Describe the morphology of the erythrocytes.
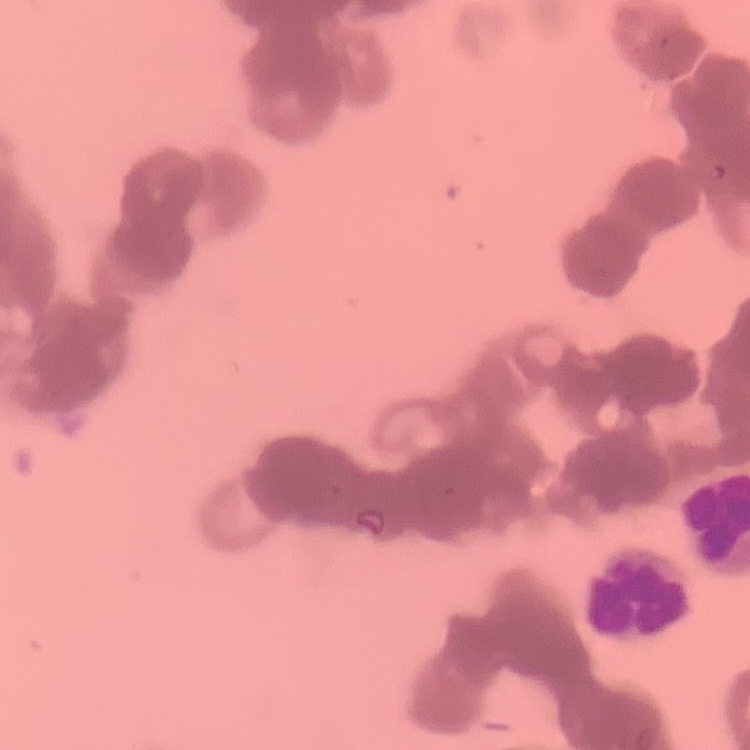

They show rouleaux formation.

Field's or Giemsa stain. One tile cut from a larger photomicrograph. Thin blood film.